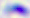

Toxoplasma gondii is seen. Captured at 400x magnification. Photomicrograph.